Outline each uninfected red blood cell.
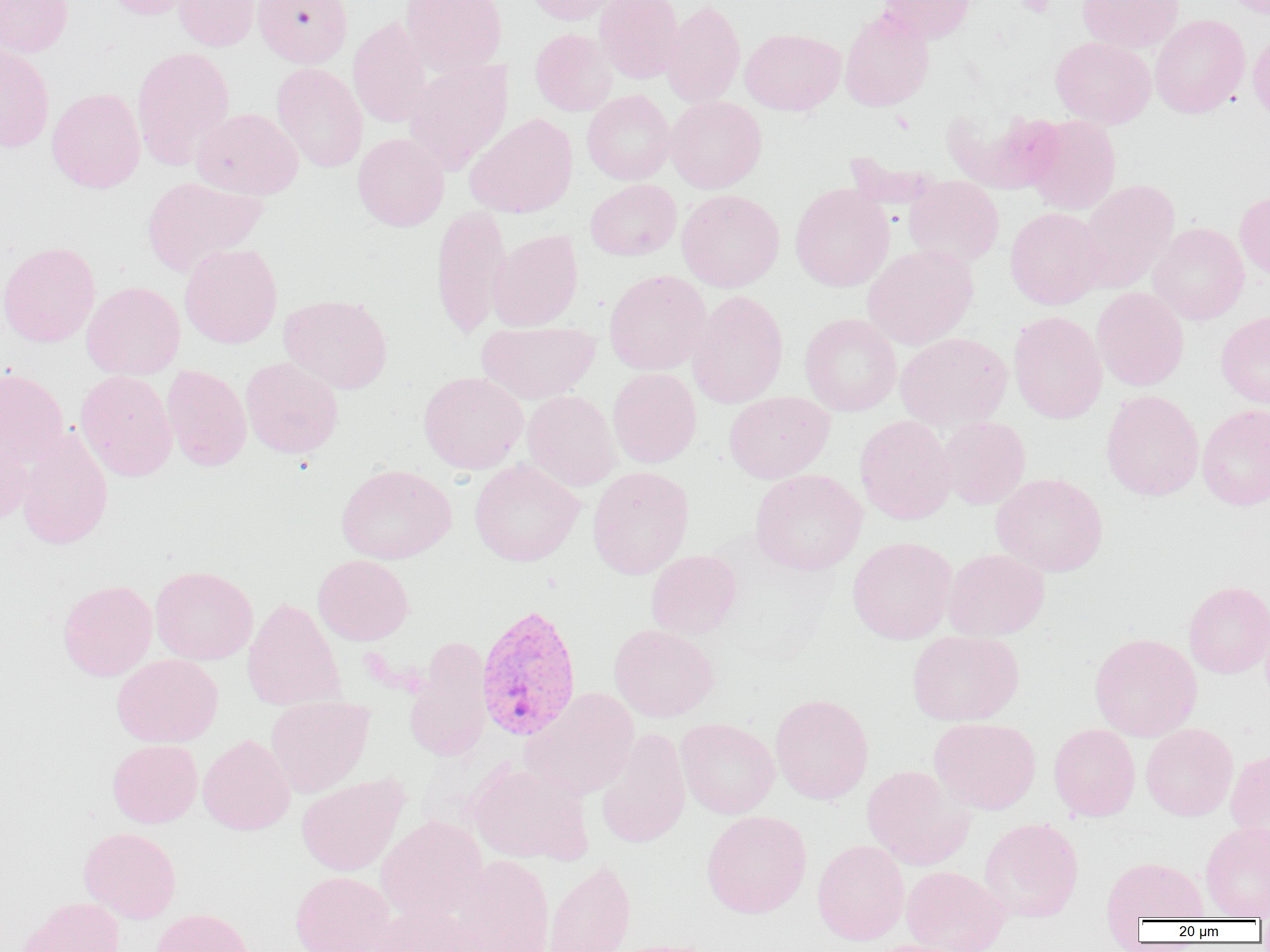
Approximate bounding boxes as (x1, y1, x2, y2) in pixels.
Uninfected red blood cells: (0, 0, 73, 56), (102, 0, 204, 20), (173, 0, 263, 51), (253, 0, 352, 67), (401, 0, 507, 76), (525, 0, 627, 25), (594, 0, 684, 83), (878, 0, 975, 43), (1077, 0, 1184, 53), (1220, 0, 1270, 19), (661, 1, 745, 107), (840, 8, 934, 111), (1150, 14, 1250, 118), (348, 17, 432, 128), (1248, 27, 1270, 124), (740, 28, 845, 115), (531, 29, 617, 116), (1050, 36, 1156, 128), (0, 43, 54, 152), (132, 46, 235, 169), (404, 59, 514, 174), (272, 63, 368, 173), (47, 87, 146, 193), (582, 90, 676, 184), (666, 96, 767, 193), (941, 106, 1063, 194), (192, 108, 303, 199), (464, 113, 578, 218), (1025, 116, 1121, 215), (352, 133, 449, 231), (904, 175, 1004, 268), (141, 176, 268, 276), (585, 179, 681, 260), (1077, 179, 1180, 293), (790, 184, 894, 292), (677, 189, 784, 292), (1235, 191, 1270, 282), (430, 205, 511, 340), (1005, 207, 1106, 309), (1148, 222, 1249, 325), (487, 229, 583, 331), (0, 242, 100, 347), (179, 243, 282, 348), (862, 244, 978, 350), (604, 270, 711, 375), (82, 281, 185, 380), (1092, 287, 1189, 391), (687, 290, 788, 408), (279, 293, 392, 394), (1008, 310, 1107, 424), (1216, 311, 1270, 408), (800, 313, 901, 416), (476, 321, 600, 404), (895, 332, 1012, 431), (240, 357, 344, 458), (162, 364, 251, 471), (0, 367, 69, 473), (607, 368, 701, 468), (75, 370, 177, 481), (418, 371, 528, 473), (523, 390, 621, 491), (1100, 390, 1204, 501), (724, 391, 834, 483), (1197, 404, 1270, 510), (855, 415, 956, 524), (937, 417, 1030, 509), (0, 419, 34, 526), (15, 428, 113, 551), (469, 459, 584, 566), (335, 464, 456, 564), (588, 466, 694, 579), (749, 469, 867, 575), (991, 473, 1108, 576), (847, 536, 957, 644), (943, 548, 1050, 640), (646, 550, 742, 638), (313, 554, 413, 645), (150, 566, 258, 665), (57, 579, 157, 681), (1183, 581, 1270, 678), (242, 597, 346, 711), (609, 624, 719, 721), (907, 631, 1024, 726), (1089, 632, 1202, 741), (405, 637, 492, 762), (111, 654, 223, 747), (521, 688, 640, 801), (770, 693, 873, 804), (266, 697, 374, 797), (929, 717, 1040, 814), (676, 718, 779, 819), (1049, 723, 1140, 821), (1141, 723, 1238, 821), (596, 727, 691, 849), (198, 734, 295, 835), (107, 739, 202, 828), (1225, 748, 1270, 849), (467, 762, 593, 865), (862, 765, 974, 870), (296, 774, 408, 876), (701, 810, 812, 918), (375, 816, 488, 923), (979, 817, 1084, 923), (1200, 821, 1270, 920), (79, 827, 181, 923), (812, 840, 909, 945), (454, 855, 555, 952), (1101, 856, 1208, 925), (543, 860, 635, 952), (901, 865, 1010, 952), (290, 871, 395, 952), (18, 896, 125, 952), (369, 903, 492, 952), (150, 908, 254, 952), (606, 939, 725, 952), (865, 939, 973, 952).

Platelet locations: (1015, 0, 1055, 17). Plasmodium vivax-infected red blood cell locations: (475, 603, 583, 741). Slide-level diagnosis: Plasmodium vivax. Light microscopy. 1000x magnification. Thin blood smear. Image is 1270×952 pixels. Single field of view.